Report the malaria status of this cell.
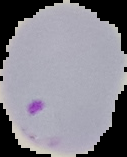
Parasitized.

Segmented cell region on a black background. From a thin blood film. Image is 127×157 pixels.